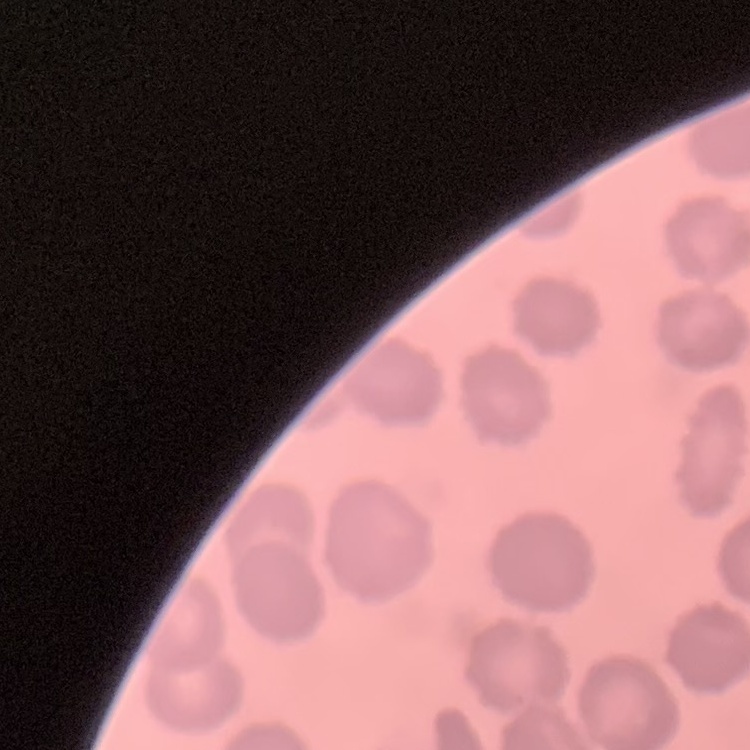
The red blood cells show no rouleaux formation. Thin blood film. Square crop of a larger photomicrograph. Field's or Giemsa stain.